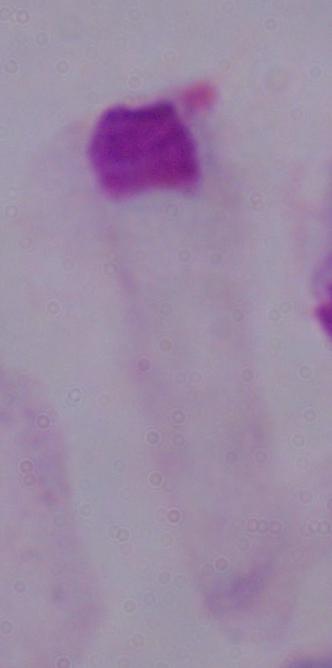
Photomicrograph. 1000x magnification. A trichomonad is shown.